Name the parasite shown.
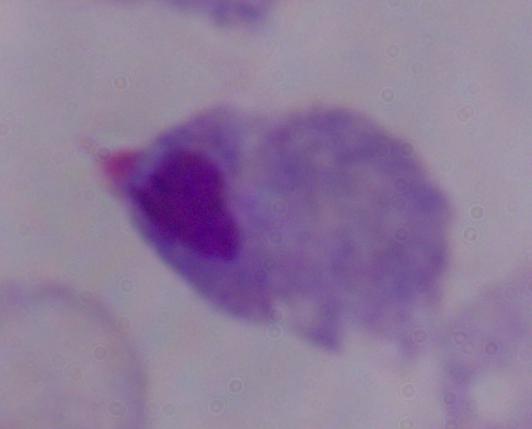
A trichomonad.

{
  "modality": "micrograph",
  "magnification": "1000x"
}